Classify this cell by malaria status.
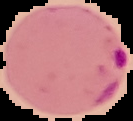

Parasitized.

image type = segmented cell region with the area outside set to black
image size = 133×121 pixels
preparation = thin blood film